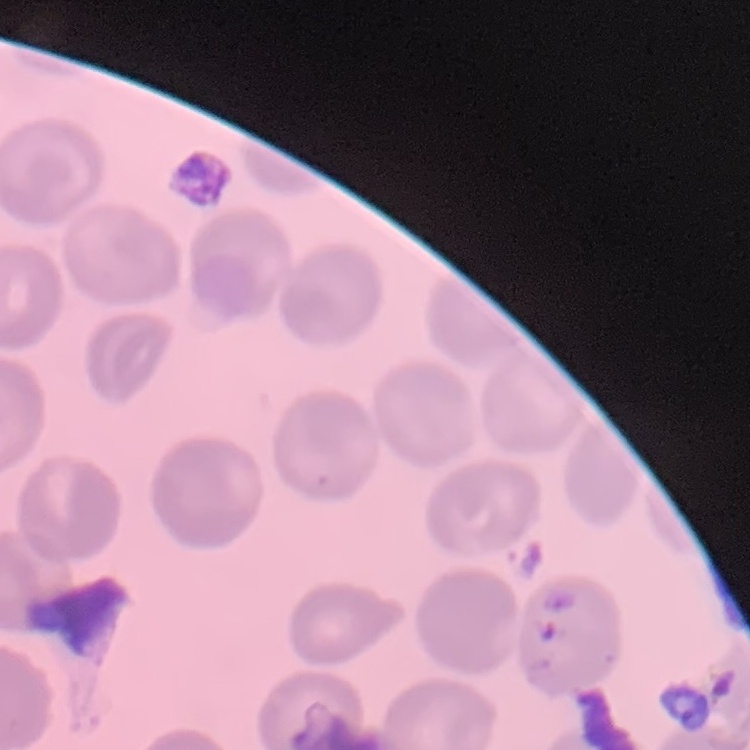

{
  "red_blood_cell_morphology": "no rouleaux formation",
  "stain": "Field's or Giemsa",
  "image_type": "one tile cut from a larger photomicrograph",
  "preparation": "thin blood smear"
}